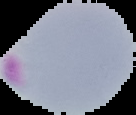
image size = 136×115 pixels
result = malaria parasites identified
image type = segmented cell region with the area outside set to black
preparation = thin blood film